Identify the parasite.
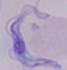

A trypanosome.

Summary:
  - Modality: photomicrograph
  - Magnification: 1000x